Report the malaria status.
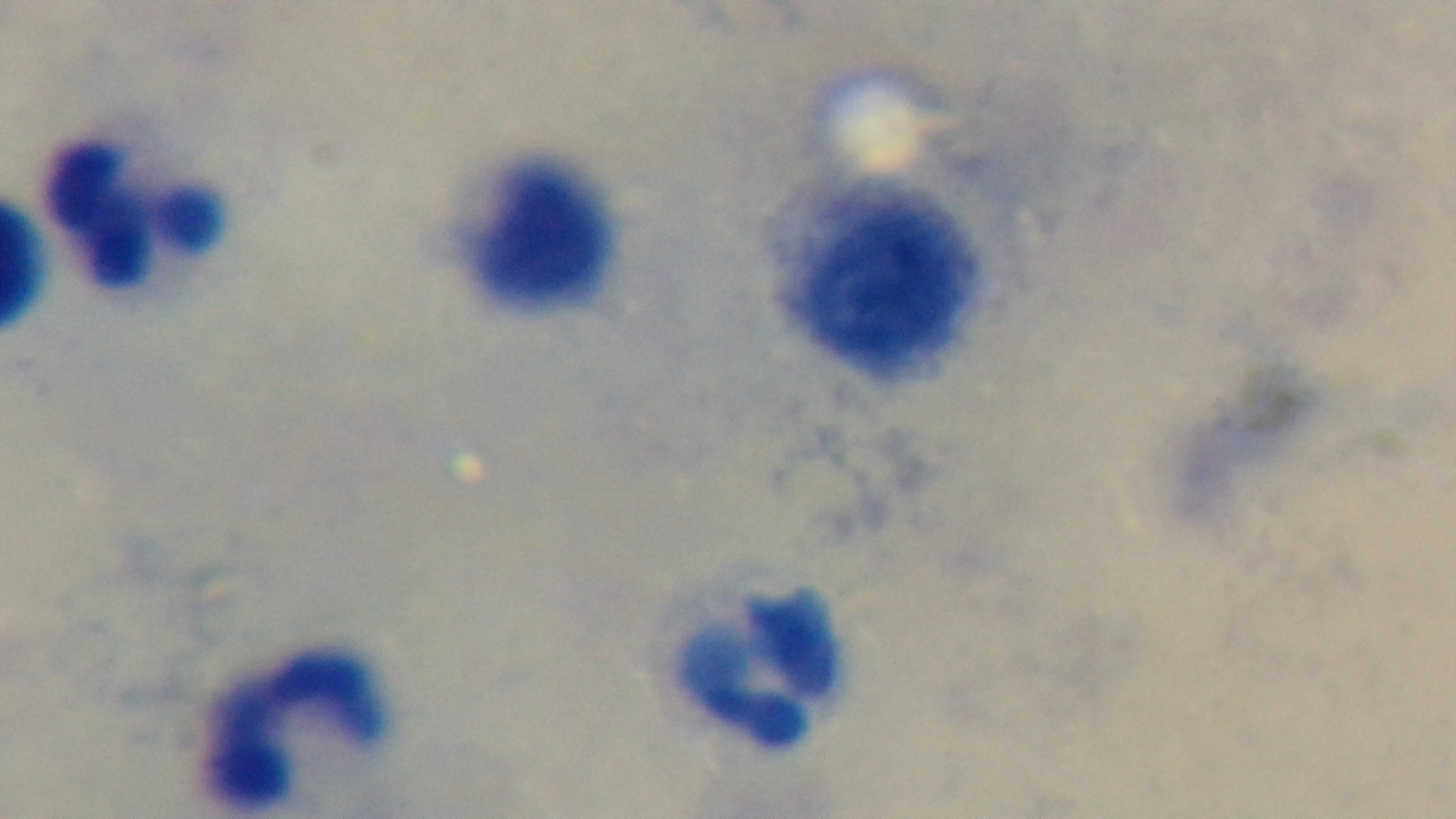

It is uninfected.

Giemsa-stained. One field from the slide. 100x oil-immersion objective. Mounted 4K digital camera. Preparation: thick smear. Light microscopy.